Locate every Plasmodium parasite and every leukocyte.
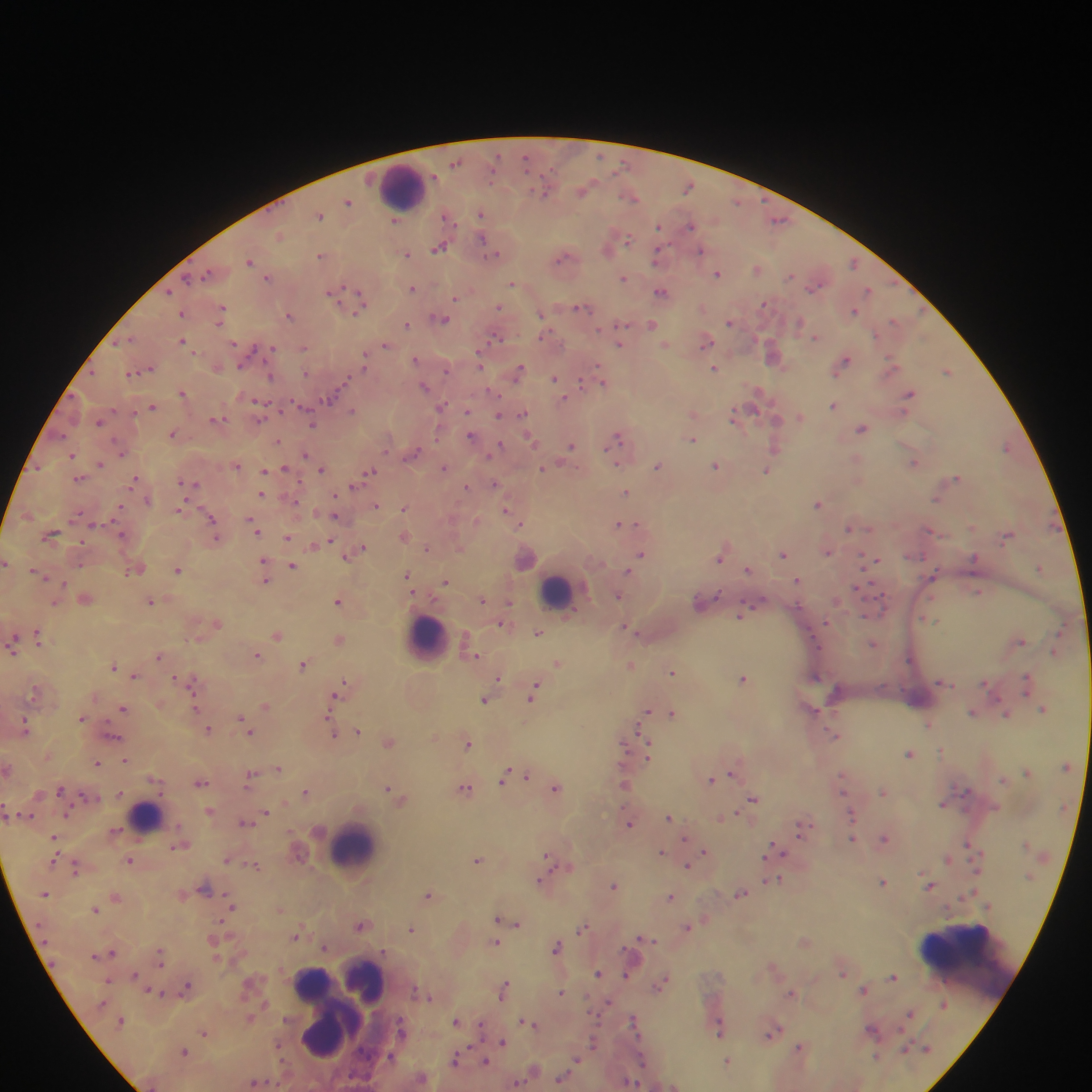

Approximate centers as x y in pixels.
Plasmodium parasites: 600 156; 525 159; 455 162; 688 186; 583 190; 544 193; 631 197; 348 201; 737 202; 481 214; 320 215; 446 215; 779 219; 395 220; 659 226; 690 226; 280 236; 483 238; 628 240; 439 248; 701 251; 407 254; 495 255; 320 256; 658 256; 563 257; 250 260; 853 263; 757 269; 207 273; 717 274; 790 276; 187 278; 268 278; 623 278; 512 284; 816 287; 413 288; 868 290; 169 291; 661 291; 331 293; 361 298; 456 298; 764 304; 499 307; 581 307; 222 308; 358 311; 854 311; 182 314; 541 314; 289 315; 443 319; 894 321; 220 322; 730 322; 799 324; 408 325; 622 325; 653 325; 496 337; 815 337; 129 339; 183 341; 706 341; 117 342; 621 344; 234 345; 385 345; 665 345; 273 348; 304 348; 773 356; 364 357; 415 359; 845 361; 479 362; 892 362; 241 366; 362 366; 715 368; 447 369; 518 371; 947 371; 131 373; 306 373; 270 376; 554 378; 581 382; 603 382; 424 387; 183 393; 758 393; 909 394; 332 396; 564 398; 260 403; 442 406; 834 406; 153 407; 353 410; 467 411; 522 414; 498 415; 733 416; 800 416; 261 418; 216 419; 777 420; 99 421; 312 425; 862 429; 173 434; 62 435; 471 437; 618 437; 530 439; 692 439; 278 441; 572 445; 499 446; 776 447; 1006 447; 122 453; 413 453; 305 454; 72 455; 101 463; 616 463; 913 463; 38 466; 237 466; 657 466; 715 466; 444 467; 543 467; 284 469; 321 469; 265 471; 767 471; 370 472; 956 478; 79 479; 134 480; 183 482; 193 484; 495 484; 357 485; 466 487; 626 492; 261 493; 335 497; 936 499; 148 500; 817 504; 376 505; 404 508; 180 509; 505 510; 335 516; 211 519; 520 524; 622 524; 848 528; 256 530; 51 534; 122 534; 404 536; 215 537; 287 537; 1007 537; 331 541; 81 542; 313 546; 428 548; 361 549; 827 551; 355 552; 641 553; 783 554; 347 555; 719 558; 974 558; 874 561; 5 563; 80 564; 292 566; 264 567; 1039 567; 132 571; 177 571; 629 571; 749 571; 37 572; 934 573; 265 575; 408 576; 798 580; 445 581; 856 589; 978 592; 716 595; 619 596; 86 600; 482 600; 150 601; 338 602; 55 603; 509 604; 741 613; 929 620; 826 623; 217 624; 503 625; 627 629; 538 633; 277 635; 38 636; 339 639; 1021 640; 873 643; 13 647; 1054 653; 257 655; 158 656; 475 656; 558 663; 303 665; 629 665; 114 666; 672 671; 135 675; 499 677; 742 678; 191 681; 1026 682; 987 685; 342 686; 34 692; 533 692; 334 698; 485 700; 194 706; 265 707; 123 709; 1044 709; 647 711; 973 712; 672 713; 328 714; 1007 714; 82 718; 242 718; 928 725; 246 726; 26 728; 210 729; 357 731; 250 732; 334 735; 836 736; 113 737; 389 742; 467 743; 624 746; 648 751; 909 754; 125 759; 97 763; 279 767; 1027 771; 731 773; 526 776; 250 777; 503 777; 1003 779; 711 780; 201 783; 624 783; 388 788; 466 788; 60 789; 556 789; 306 792; 843 792; 882 792; 86 795; 753 799; 943 803; 210 810; 266 812; 725 816; 669 817; 245 822; 629 823; 801 828; 54 838; 853 838; 885 838; 968 844; 180 846; 776 850; 704 851; 661 852; 549 858; 947 859; 226 860; 477 860; 129 861; 253 865; 689 865; 75 867; 541 880; 775 880; 882 882; 930 885; 614 886; 206 889; 428 894; 740 894; 116 896; 670 898; 231 907; 95 909; 498 919; 518 923; 360 926; 583 927; 688 927; 411 929; 297 934; 643 938; 496 942; 556 946; 324 948; 112 953; 160 956; 598 973; 843 974; 135 975; 626 975; 893 977; 108 980; 661 984; 186 988; 504 989; 864 989; 157 992; 561 992; 790 993; 909 1013; 633 1020; 121 1021; 456 1021; 526 1022; 401 1028; 872 1029; 719 1030; 204 1032; 772 1033; 503 1042; 593 1043; 799 1048; 183 1051; 390 1056; 876 1057; 576 1059; 456 1060; 642 1060; 485 1062; 728 1062; 561 1078; 256 1082; 629 1082; 518 1083; 674 1086.
Leukocytes: 403 190; 557 591; 427 635; 146 817; 352 848; 961 969; 368 983; 314 984; 340 988; 331 1031.

One field of view. Sample from Ghana. Image is 1092×1092 pixels. Photographed through a microscope with a mobile-phone camera. Thick blood film.